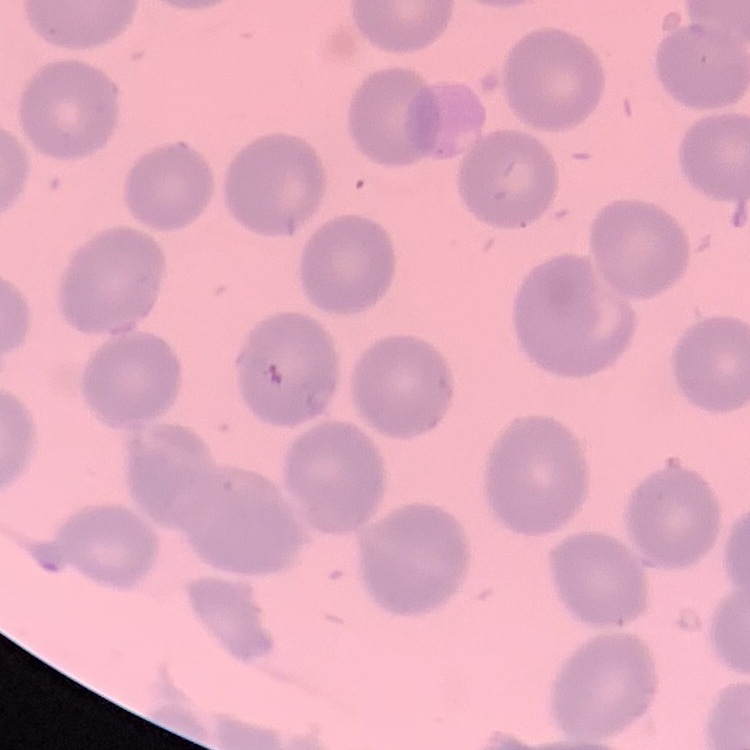
{
  "red_blood_cell_morphology": "no rouleaux formation",
  "preparation": "thin peripheral smear",
  "image_type": "one tile cut from a larger photomicrograph",
  "stain": "Field's or Giemsa"
}